State which parasite is depicted.
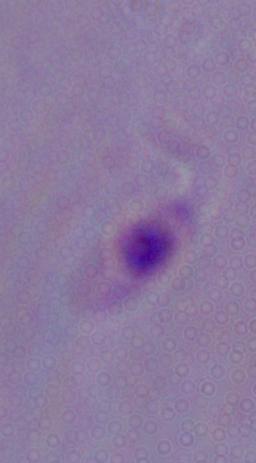

This is Leishmania.

Captured at 1000x magnification. Micrograph.